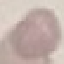
Summary:
  - Result: no malaria parasites detected
  - Capture: smartphone camera at the microscope eyepiece
  - Preparation: thin blood film
  - Image type: automatically extracted cell patch, resized to 64 × 64 pixels
  - Stain: Giemsa